Outline each uninfected red blood cell.
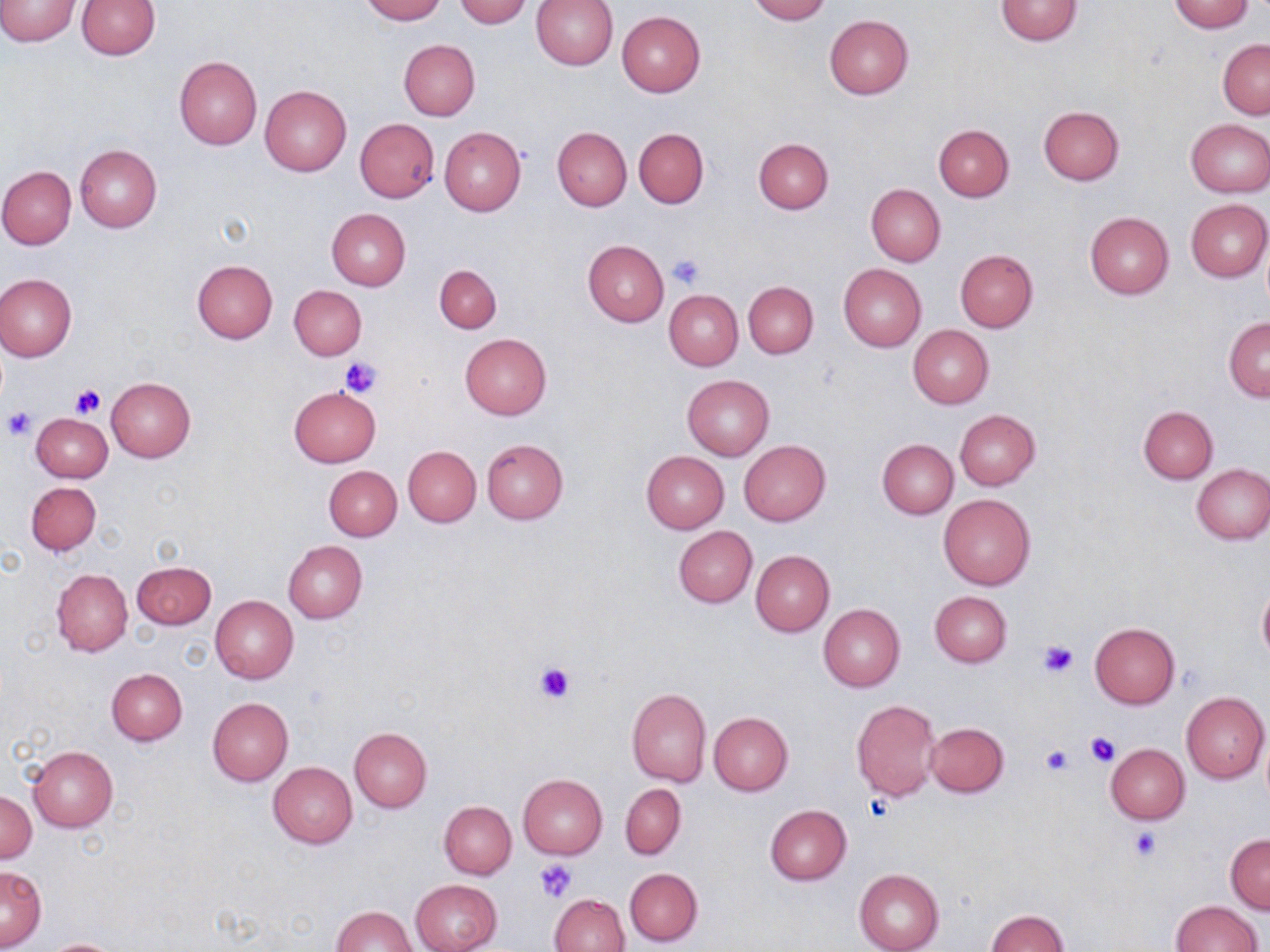
Approximate bounding boxes as (x1,y1)-(x2,y2) corner pairs in pixels.
Uninfected red blood cells: (0,0)-(80,46), (359,0)-(447,23), (455,0)-(533,27), (747,0)-(830,23), (994,0)-(1083,45), (1166,0)-(1255,32), (75,1)-(159,59), (532,1)-(618,70), (617,11)-(705,96), (824,15)-(913,99), (1218,38)-(1270,118), (399,40)-(480,121), (174,56)-(262,150), (260,84)-(351,176), (1038,106)-(1124,185), (354,118)-(439,202), (1185,119)-(1270,196), (933,124)-(1014,202), (439,127)-(526,216), (552,127)-(632,211), (633,128)-(709,208), (754,137)-(833,214), (75,144)-(162,231), (0,166)-(76,249), (866,184)-(946,265), (1185,198)-(1270,282), (326,208)-(410,290), (1084,212)-(1174,298), (581,239)-(669,326), (955,250)-(1037,332), (192,259)-(278,343), (434,264)-(502,334), (838,264)-(927,351), (0,274)-(76,360), (743,281)-(819,358), (289,284)-(367,360), (664,289)-(743,370), (1223,316)-(1270,402), (909,326)-(993,408), (459,334)-(551,420), (682,374)-(774,460), (106,377)-(195,461), (289,386)-(381,467), (1139,406)-(1218,483), (955,409)-(1040,489), (32,413)-(113,483), (481,438)-(569,523), (738,439)-(831,525), (878,440)-(957,518), (402,446)-(481,527), (641,451)-(729,532), (1191,464)-(1269,545), (324,465)-(401,540), (26,481)-(100,556), (938,493)-(1036,591), (673,526)-(758,607), (283,540)-(367,623), (750,550)-(834,636), (131,561)-(216,629), (51,568)-(132,657), (1256,583)-(1270,664), (930,591)-(1012,667), (212,595)-(298,683), (819,603)-(905,691), (1089,622)-(1180,709), (105,668)-(188,745), (626,686)-(711,787), (1180,691)-(1269,784), (208,697)-(294,786), (851,699)-(941,800), (708,712)-(793,796), (925,721)-(1009,797), (349,727)-(432,811), (1105,744)-(1190,824), (28,746)-(118,832), (268,761)-(357,848), (518,774)-(607,859), (620,784)-(686,859), (0,791)-(37,864), (439,801)-(516,879), (764,805)-(851,885), (1226,834)-(1270,914), (1,866)-(46,950), (624,868)-(702,946), (854,868)-(945,952), (411,879)-(501,952), (549,893)-(629,952), (1170,901)-(1263,951), (331,906)-(416,951), (986,909)-(1068,952), (41,938)-(128,952).

Summary:
  - Platelet locations: (667,253)-(705,289), (340,356)-(383,398), (71,384)-(106,418), (2,406)-(36,440), (1037,640)-(1078,677), (533,659)-(577,705), (1085,732)-(1120,768), (1041,744)-(1073,774), (1129,826)-(1162,862), (535,859)-(575,902)
  - Slide-level diagnosis: negative for blood parasites
  - Field of view: one of a larger specimen
  - Modality: optical microscopy
  - Stain: May-Grünwald-Giemsa
  - Magnification: 1000x
  - Image size: 1270×952 pixels
  - Preparation: thin blood smear